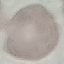
malaria status = uninfected
preparation = thin blood smear
stain = Giemsa
image type = automatically extracted cell patch, resized to 64 × 64 pixels
capture = smartphone camera at the microscope eyepiece